Name the blood parasite species.
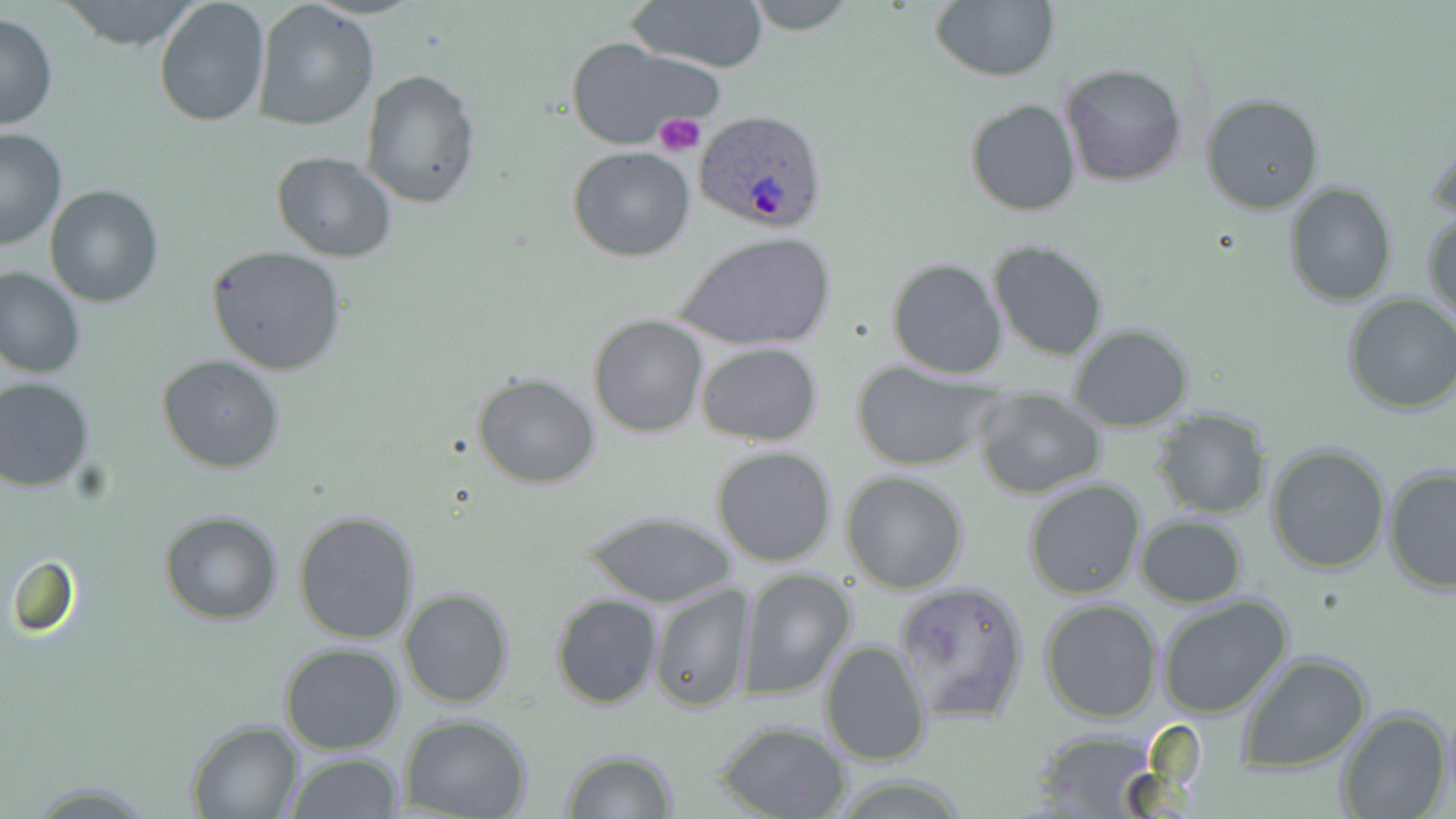
Plasmodium ovale.

Approximate bounding boxes as [x1, y1, x2, y2] in pixels. Uninfected red blood cell locations: [55, 0, 205, 51], [153, 0, 270, 126], [745, 0, 858, 35], [930, 0, 1060, 83], [628, 1, 769, 74], [255, 2, 380, 132], [0, 13, 59, 132], [565, 37, 725, 152], [1060, 62, 1187, 187], [359, 70, 482, 207], [1201, 94, 1324, 215], [964, 97, 1082, 216], [1426, 124, 1456, 227], [0, 126, 69, 250], [568, 146, 695, 262], [271, 152, 398, 260], [1284, 181, 1396, 305], [43, 183, 164, 307], [1424, 210, 1456, 330], [676, 234, 835, 352], [988, 241, 1109, 363], [207, 246, 349, 375], [886, 257, 1008, 381], [0, 266, 86, 381], [1343, 292, 1456, 416], [589, 315, 709, 438], [1068, 322, 1195, 430], [696, 343, 822, 445], [157, 354, 285, 474], [850, 361, 1000, 472], [472, 371, 601, 489], [0, 377, 97, 491], [973, 389, 1107, 499], [1152, 409, 1272, 519], [1266, 442, 1393, 575], [710, 445, 839, 567], [1383, 465, 1455, 597], [841, 471, 969, 594], [1024, 479, 1147, 600], [580, 509, 737, 608], [159, 511, 283, 625], [293, 512, 421, 644], [1134, 514, 1248, 607], [9, 555, 77, 636], [737, 569, 856, 699], [894, 579, 1029, 727], [649, 583, 753, 715], [398, 587, 515, 708], [551, 593, 663, 710], [1156, 595, 1295, 719], [1040, 598, 1163, 722], [818, 639, 932, 768], [279, 642, 406, 754], [1238, 653, 1373, 774], [1334, 707, 1452, 819], [399, 715, 533, 819], [187, 720, 304, 818], [714, 720, 853, 818], [1029, 727, 1165, 816], [561, 749, 678, 819], [286, 751, 405, 819]. Plasmodium ovale-infected red blood cell locations: [692, 109, 832, 230]. Platelet locations: [652, 113, 705, 157]. Optical microscopy. One field of a larger specimen. Image is 1456×819 pixels. Thin blood smear. Captured at 1000x magnification. May-Grünwald-Giemsa stain.